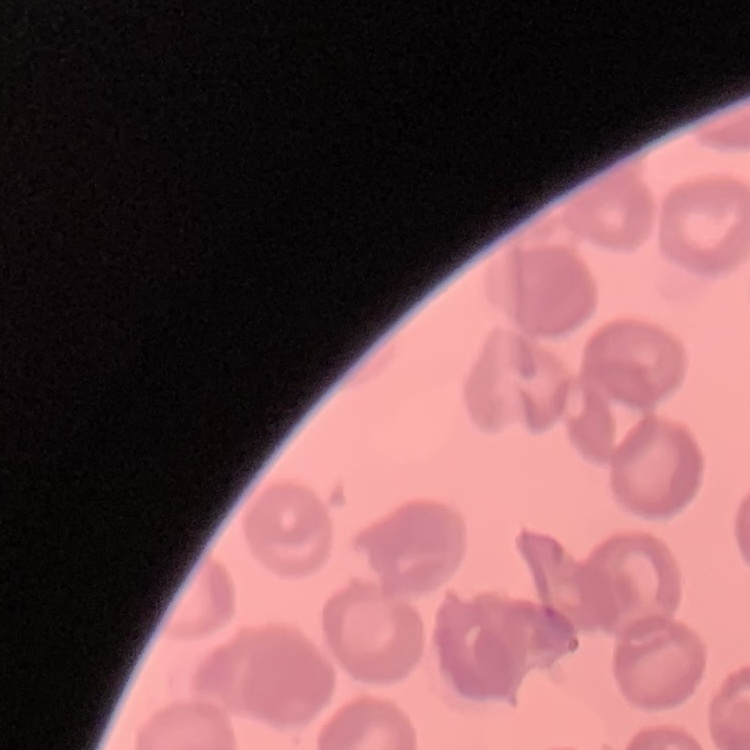
{
  "erythrocyte_morphology": "no rouleaux formation",
  "image_type": "square crop of a larger photomicrograph",
  "stain": "Field's or Giemsa",
  "preparation": "thin blood smear"
}